State which cell type is depicted.
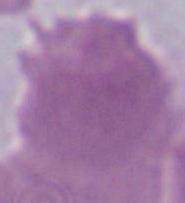
An erythrocyte.

Photomicrograph. Captured at 1000x magnification.